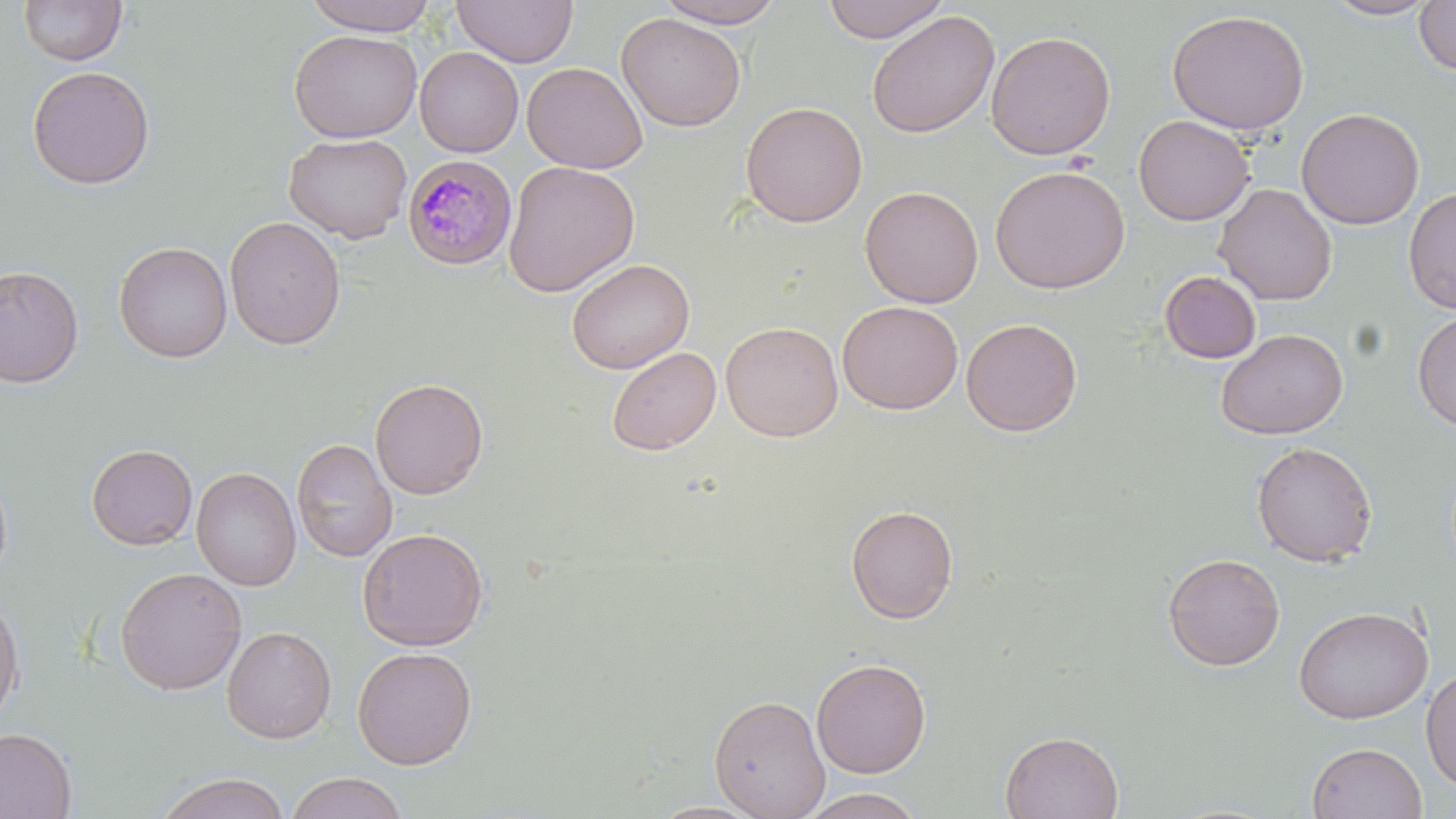
slide-level diagnosis = Plasmodium malariae
uninfected red blood cell locations = approximate bounding boxes as (x1, y1, x2, y2) in pixels: (18, 0, 127, 66), (301, 0, 440, 35), (452, 0, 578, 67), (655, 0, 788, 28), (821, 0, 950, 43), (1321, 0, 1441, 21), (1414, 1, 1456, 76), (1166, 9, 1311, 136), (866, 10, 1000, 139), (616, 12, 746, 132), (289, 29, 422, 142), (985, 30, 1117, 160), (415, 47, 524, 157), (522, 62, 647, 174), (27, 65, 156, 190), (740, 101, 867, 228), (1296, 107, 1425, 230), (1133, 115, 1255, 226), (284, 132, 412, 244), (503, 161, 639, 297), (989, 165, 1130, 294), (1213, 183, 1336, 305), (859, 185, 983, 308), (1403, 186, 1456, 315), (225, 216, 346, 349), (113, 241, 232, 363), (567, 258, 694, 374), (0, 264, 83, 388), (1159, 271, 1262, 364), (837, 300, 963, 414), (1412, 311, 1456, 432), (961, 317, 1083, 436), (720, 321, 843, 442), (1215, 328, 1348, 440), (607, 346, 721, 456), (370, 377, 489, 499), (292, 438, 397, 562), (1250, 441, 1378, 567), (86, 443, 198, 550), (0, 464, 13, 592), (191, 466, 301, 591), (845, 504, 958, 624), (356, 527, 489, 650), (1162, 552, 1285, 671), (115, 566, 247, 694), (0, 594, 25, 723), (1293, 605, 1433, 724), (222, 625, 336, 744), (353, 646, 477, 770), (811, 657, 931, 778), (1421, 668, 1456, 791), (708, 694, 830, 818), (0, 727, 77, 818), (1000, 730, 1124, 818), (1306, 742, 1427, 819), (155, 772, 291, 819), (285, 772, 408, 819), (800, 788, 925, 819)
stain = May-Grünwald-Giemsa
magnification = 1000x
preparation = thin blood smear
field of view = one of a larger specimen
Plasmodium malariae-infected red blood cell locations = approximate bounding boxes as (x1, y1, x2, y2) in pixels: (401, 154, 518, 270)
modality = light microscopy
image size = 1456×819 pixels